Report the malaria status of this cell.
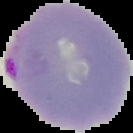
Parasitized.

From a thin blood smear. Segmented cell region on a black background. Image is 133×133 pixels.